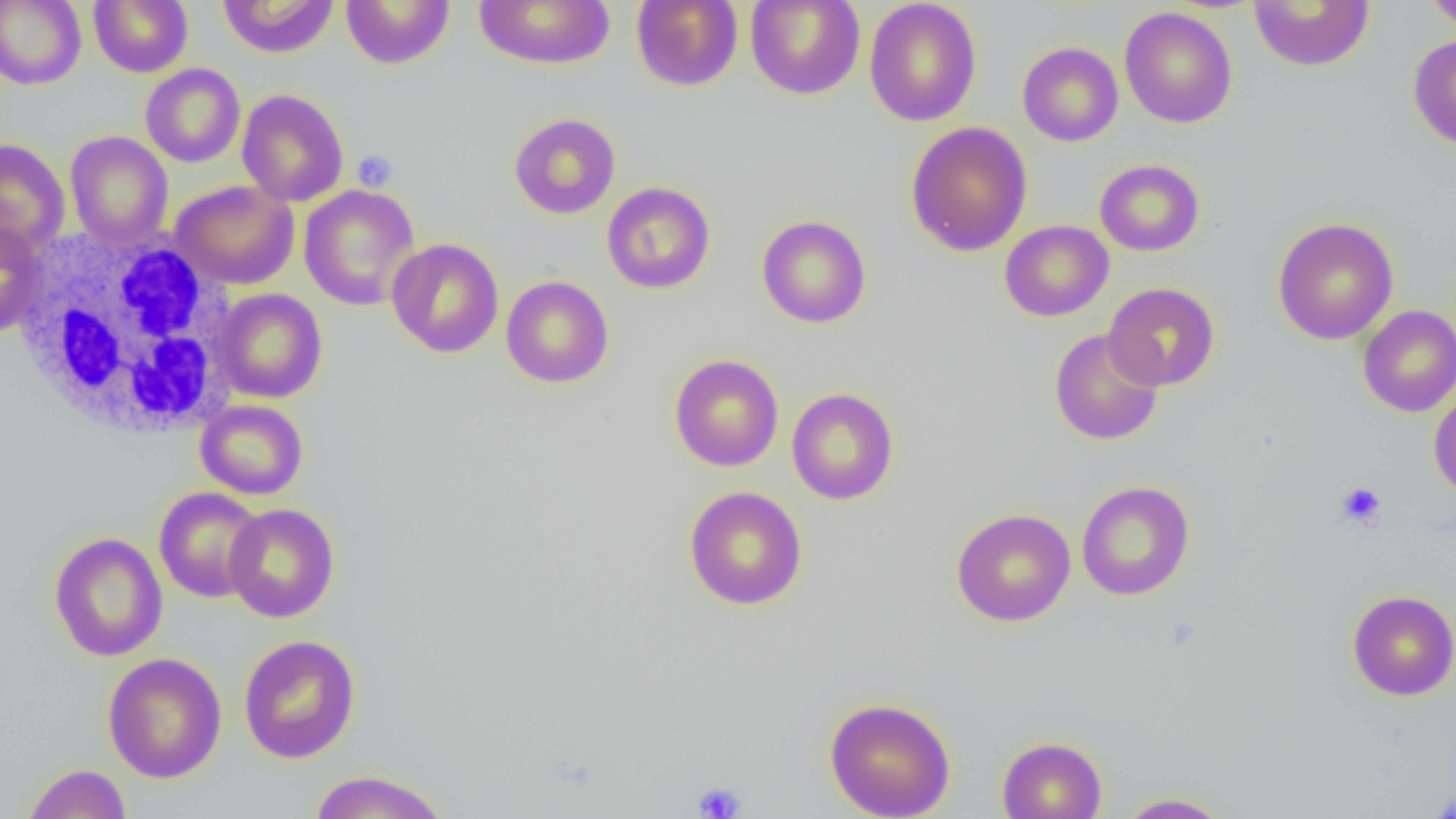 Approximate bounding boxes as (x1, y1, x2, y2) in pixels. White blood cell locations: (16, 228, 238, 440). Platelet locations: (352, 149, 398, 192), (1335, 482, 1387, 530), (691, 781, 746, 819). Uninfected red blood cell locations: (0, 0, 86, 90), (89, 0, 192, 77), (217, 0, 339, 58), (341, 0, 455, 69), (474, 0, 616, 69), (631, 0, 743, 91), (745, 0, 866, 100), (864, 0, 982, 127), (1424, 0, 1456, 34), (1249, 1, 1374, 72), (1119, 7, 1237, 128), (1408, 35, 1456, 151), (1017, 42, 1123, 146), (140, 63, 245, 167), (236, 89, 349, 206), (509, 113, 621, 219), (905, 122, 1032, 256), (64, 131, 173, 248), (0, 138, 71, 258), (1094, 159, 1204, 256), (171, 180, 299, 289), (602, 182, 716, 294), (299, 184, 420, 311), (757, 214, 871, 328), (1272, 217, 1399, 345), (0, 219, 48, 339), (1000, 220, 1114, 321), (386, 238, 504, 358), (501, 275, 614, 389), (1104, 282, 1219, 391), (214, 288, 327, 403), (1358, 305, 1456, 417), (1049, 328, 1164, 445), (669, 354, 784, 471), (1428, 386, 1456, 501), (786, 387, 899, 505), (195, 400, 308, 500), (1076, 481, 1195, 601), (684, 486, 808, 610), (153, 487, 267, 603), (224, 503, 340, 623), (951, 507, 1076, 627), (49, 532, 168, 662), (1347, 590, 1456, 701), (238, 634, 361, 764), (103, 652, 228, 783), (824, 696, 956, 818), (997, 736, 1107, 819), (22, 763, 132, 819), (308, 769, 451, 818), (1428, 784, 1456, 818), (1115, 792, 1234, 818). Slide-level diagnosis: negative for blood parasites. Optical microscopy. Image is 1456×819 pixels. Thin blood film. Single field of view. 1000x magnification.